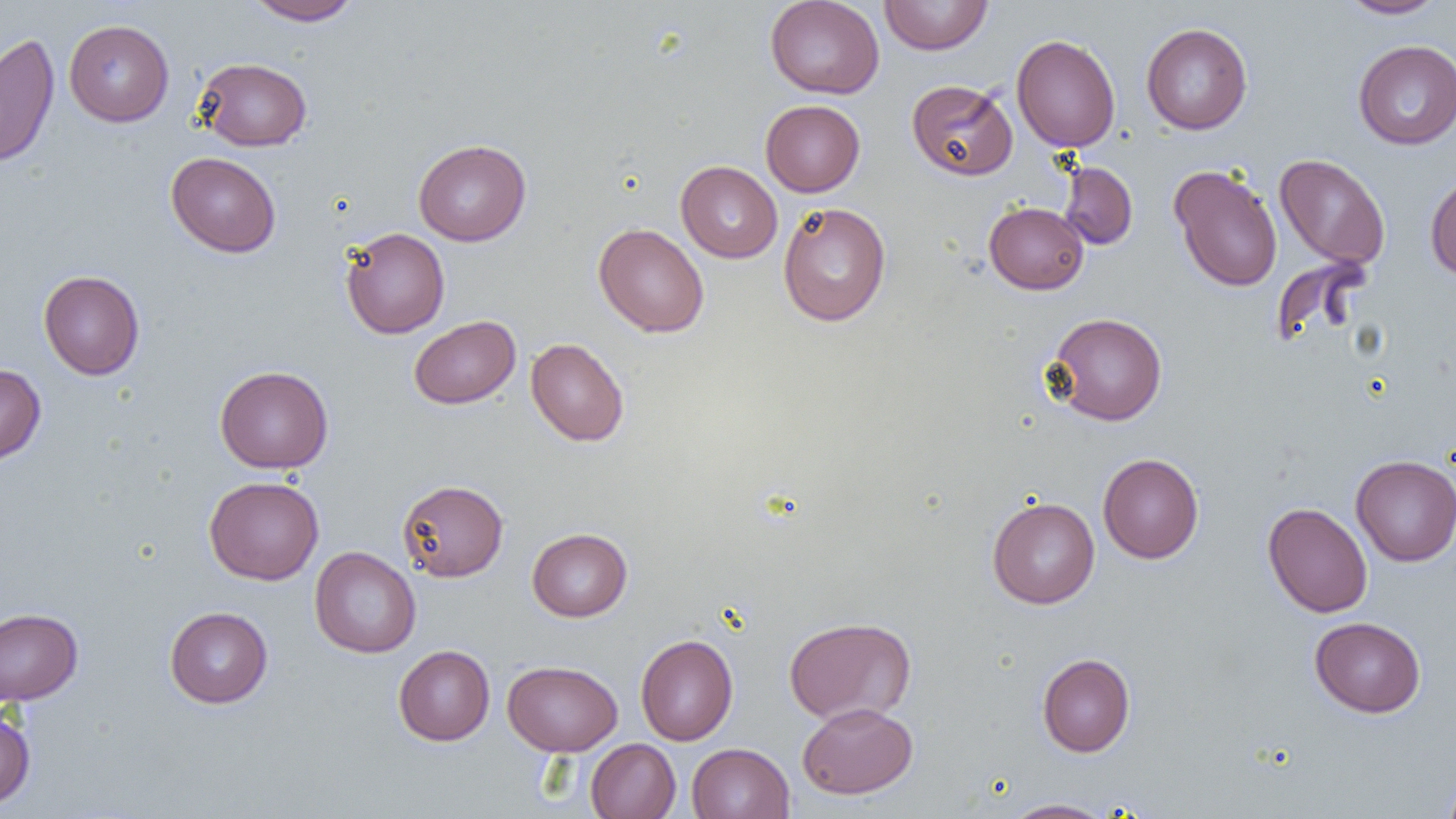

Approximate bounding boxes as (x1,y1)-(x2,y2) corner pairs in pixels. Uninfected red blood cell locations: (765,0)-(884,99), (879,0)-(993,55), (1337,0)-(1447,19), (245,1)-(363,25), (64,19)-(174,126), (1141,22)-(1253,135), (0,32)-(60,169), (1011,34)-(1120,152), (1353,40)-(1456,150), (195,57)-(312,151), (906,79)-(1018,180), (761,100)-(865,196), (413,139)-(530,246), (166,152)-(281,257), (1274,154)-(1390,270), (676,161)-(783,263), (1058,161)-(1138,250), (1169,164)-(1283,292), (1425,173)-(1456,281), (777,202)-(892,327), (984,202)-(1089,295), (593,223)-(709,337), (340,227)-(450,338), (1269,255)-(1371,350), (38,270)-(145,380), (1045,312)-(1168,426), (409,315)-(521,409), (526,338)-(629,446), (0,363)-(46,464), (215,365)-(333,473), (1097,453)-(1204,563), (1351,455)-(1456,566), (204,476)-(323,584), (397,479)-(509,582), (986,496)-(1100,609), (1262,502)-(1373,617), (527,528)-(632,621), (310,547)-(421,658), (164,606)-(273,708), (0,608)-(83,705), (784,616)-(917,725), (1309,616)-(1426,718), (635,634)-(738,745), (393,645)-(495,746), (1037,653)-(1135,757), (503,660)-(622,755), (797,702)-(917,799), (0,708)-(35,808), (585,738)-(681,819), (687,742)-(795,819), (1441,772)-(1456,819), (1002,798)-(1115,819). Slide-level diagnosis: no evidence of blood parasites. One field of a larger specimen. Optical microscopy. Image is 1456×819 pixels. 1000x magnification. Thin blood smear.